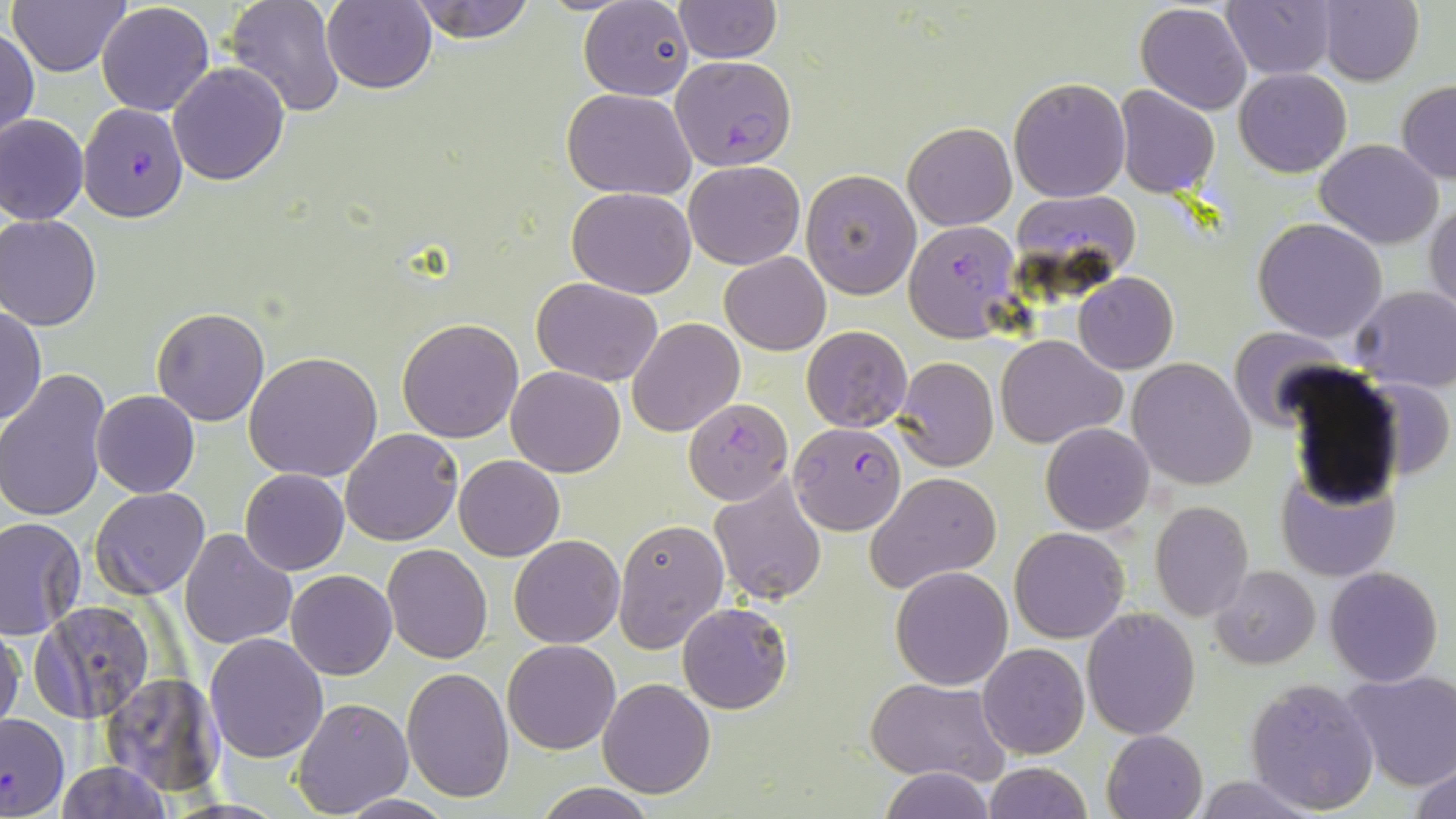
Summary:
  - Coordinate format: approximate bounding boxes as [x1, y1, x2, y2] in pixels
  - Uninfected red blood cell locations: [7, 0, 130, 75], [224, 0, 346, 117], [322, 0, 436, 93], [405, 0, 539, 42], [674, 0, 781, 63], [1221, 0, 1339, 79], [1317, 0, 1424, 86], [579, 2, 694, 101], [1134, 2, 1253, 114], [96, 3, 214, 115], [1, 30, 38, 142], [167, 61, 290, 185], [1235, 67, 1351, 176], [1008, 77, 1130, 202], [1397, 80, 1456, 184], [1116, 86, 1220, 197], [562, 89, 695, 199], [0, 113, 88, 225], [901, 122, 1016, 230], [1315, 139, 1443, 248], [683, 160, 804, 269], [802, 169, 921, 299], [568, 187, 696, 297], [1426, 200, 1456, 317], [1, 215, 101, 330], [1253, 218, 1387, 341], [720, 251, 831, 355], [1074, 272, 1178, 373], [532, 278, 662, 386], [1350, 285, 1456, 391], [1, 305, 46, 427], [152, 307, 270, 426], [397, 317, 525, 442], [628, 319, 744, 438], [802, 325, 913, 433], [1228, 326, 1347, 431], [994, 334, 1125, 449], [245, 350, 385, 482], [894, 356, 997, 471], [1128, 358, 1258, 489], [506, 366, 627, 477], [1, 369, 109, 523], [1364, 377, 1453, 482], [91, 389, 200, 497], [1042, 423, 1155, 534], [340, 428, 464, 546], [454, 455, 565, 560], [1275, 463, 1401, 583], [241, 468, 349, 575], [868, 472, 1001, 588], [712, 476, 827, 605], [91, 486, 210, 602], [1150, 500, 1253, 620], [121, 501, 276, 624], [0, 518, 86, 639], [613, 520, 728, 653], [1011, 527, 1128, 644], [178, 530, 297, 650], [509, 535, 625, 648], [384, 544, 493, 663], [1211, 564, 1320, 669], [891, 566, 1014, 690], [1324, 566, 1444, 686], [286, 569, 397, 679], [30, 600, 155, 722], [678, 602, 792, 713], [1082, 606, 1200, 739], [0, 624, 24, 732], [204, 631, 329, 762], [501, 640, 620, 755], [978, 642, 1088, 758], [401, 667, 513, 802], [1339, 671, 1455, 791], [102, 673, 224, 794], [1245, 676, 1380, 814], [597, 677, 716, 798], [864, 678, 1008, 784], [293, 697, 413, 816], [1101, 729, 1207, 819], [1411, 759, 1456, 819], [56, 760, 170, 818], [981, 762, 1092, 819], [876, 767, 994, 818], [1189, 775, 1322, 817], [532, 784, 658, 818], [333, 794, 462, 817]
  - Plasmodium falciparum-infected red blood cell locations: [673, 54, 799, 182], [78, 102, 187, 221], [904, 219, 1021, 341], [682, 398, 791, 504], [787, 420, 903, 538], [0, 711, 68, 818]
  - Slide-level diagnosis: Plasmodium falciparum
  - Image size: 1456×819 pixels
  - Magnification: 1000x
  - Field of view: single
  - Stain: May-Grünwald-Giemsa
  - Preparation: thin blood film
  - Modality: optical microscopy